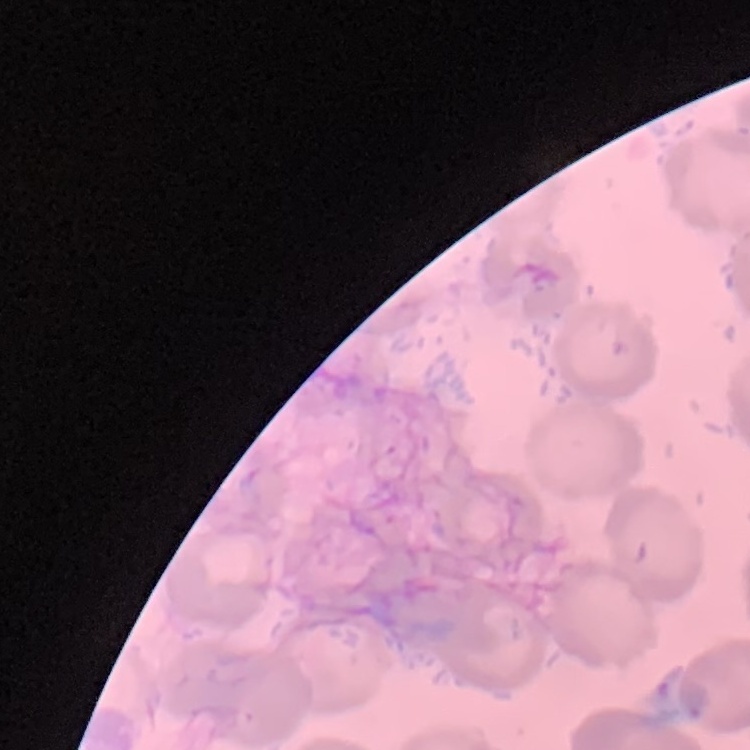

Summary:
  - Erythrocyte morphology: no rouleaux formation
  - Stain: Field's or Giemsa
  - Image type: one tile cut from a larger photomicrograph
  - Preparation: thin blood film